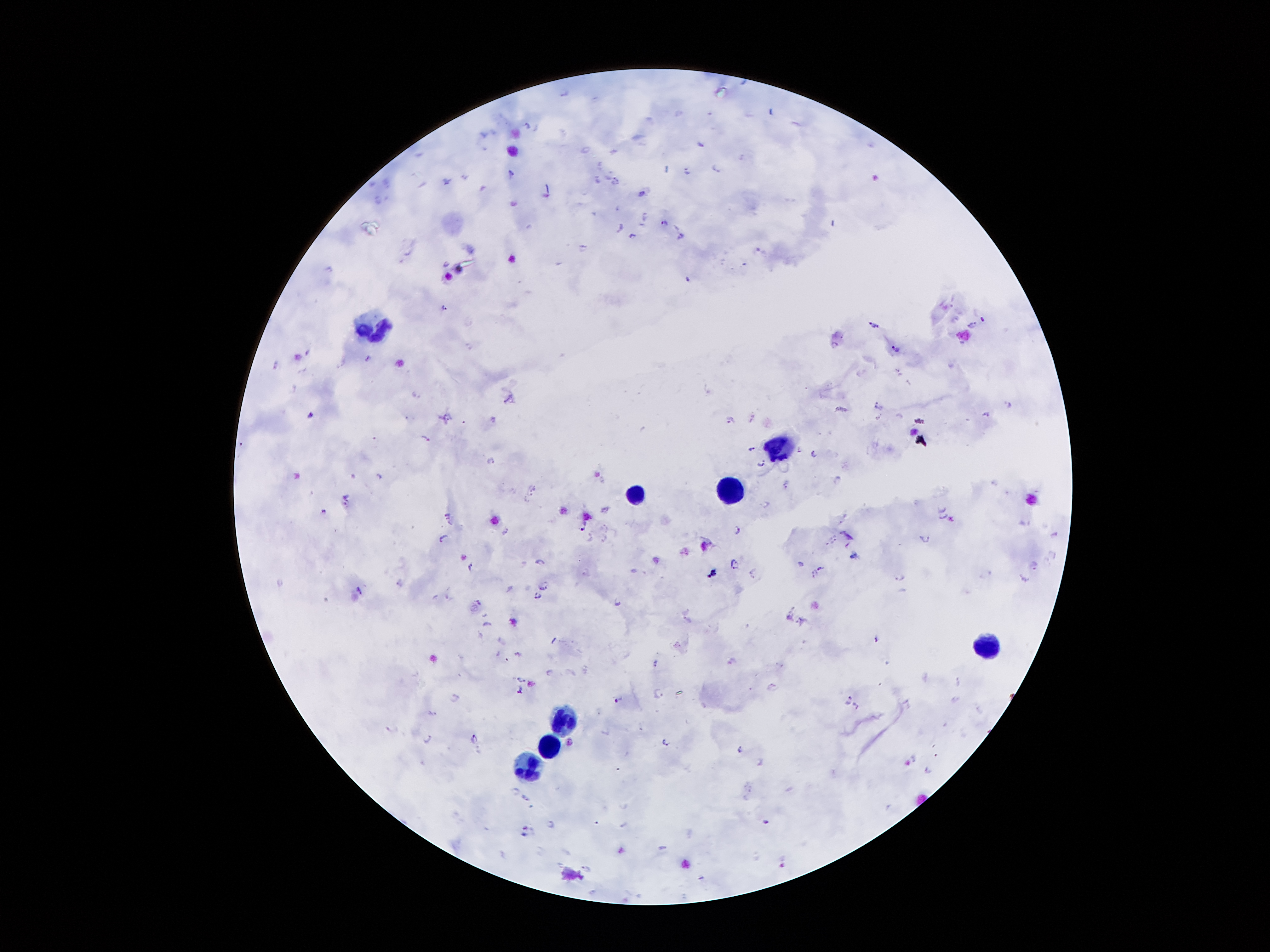
Approximate centers as {x, y} in pixels. Leukocyte locations: {370, 327}, {782, 448}, {725, 490}, {640, 494}, {985, 647}, {563, 718}, {549, 746}, {527, 767}. Plasmodium parasite locations: {527, 125}, {700, 143}, {599, 165}, {715, 167}, {666, 168}, {686, 170}, {511, 175}, {598, 178}, {446, 180}, {616, 181}, {641, 193}, {379, 201}, {513, 202}, {644, 214}, {662, 221}, {621, 225}, {633, 234}, {681, 236}, {584, 247}, {756, 249}, {446, 262}, {444, 306}, {956, 318}, {982, 318}, {872, 323}, {971, 324}, {896, 350}, {368, 356}, {278, 364}, {416, 394}, {510, 396}, {878, 403}, {1008, 403}, {312, 413}, {987, 413}, {448, 415}, {493, 418}, {731, 419}, {428, 435}, {375, 438}, {753, 448}, {800, 449}, {813, 453}, {492, 461}, {761, 463}, {379, 478}, {838, 480}, {784, 484}, {533, 489}, {347, 496}, {526, 502}, {767, 503}, {345, 505}, {942, 509}, {323, 512}, {447, 515}, {944, 517}, {584, 524}, {604, 526}, {737, 530}, {506, 531}, {593, 531}, {1054, 533}, {443, 537}, {604, 537}, {927, 537}, {833, 538}, {848, 546}, {1050, 553}, {539, 560}, {734, 562}, {801, 564}, {1032, 564}, {471, 567}, {821, 567}, {583, 571}, {752, 571}, {712, 572}, {987, 572}, {813, 573}, {900, 577}, {1025, 577}, {399, 581}, {544, 585}, {359, 589}, {537, 597}, {618, 602}, {478, 603}, {687, 611}, {484, 614}, {688, 621}, {487, 622}, {877, 639}, {678, 644}, {519, 654}, {733, 661}, {657, 662}, {548, 672}, {520, 678}, {773, 684}, {520, 689}, {659, 693}, {455, 697}, {850, 697}, {616, 700}, {856, 705}, {391, 728}, {428, 738}, {475, 738}, {664, 742}, {741, 749}, {914, 756}, {760, 762}, {927, 770}, {526, 797}, {766, 821}, {552, 824}, {525, 828}, {662, 846}, {562, 864}, {585, 867}. Giemsa stain. One field from this slide. Thick blood smear. 100x magnification. Smartphone photograph taken through the microscope eyepiece. Patient malaria status: positive for Plasmodium falciparum. Image is 1270×952 pixels.